Identify the preparation type.
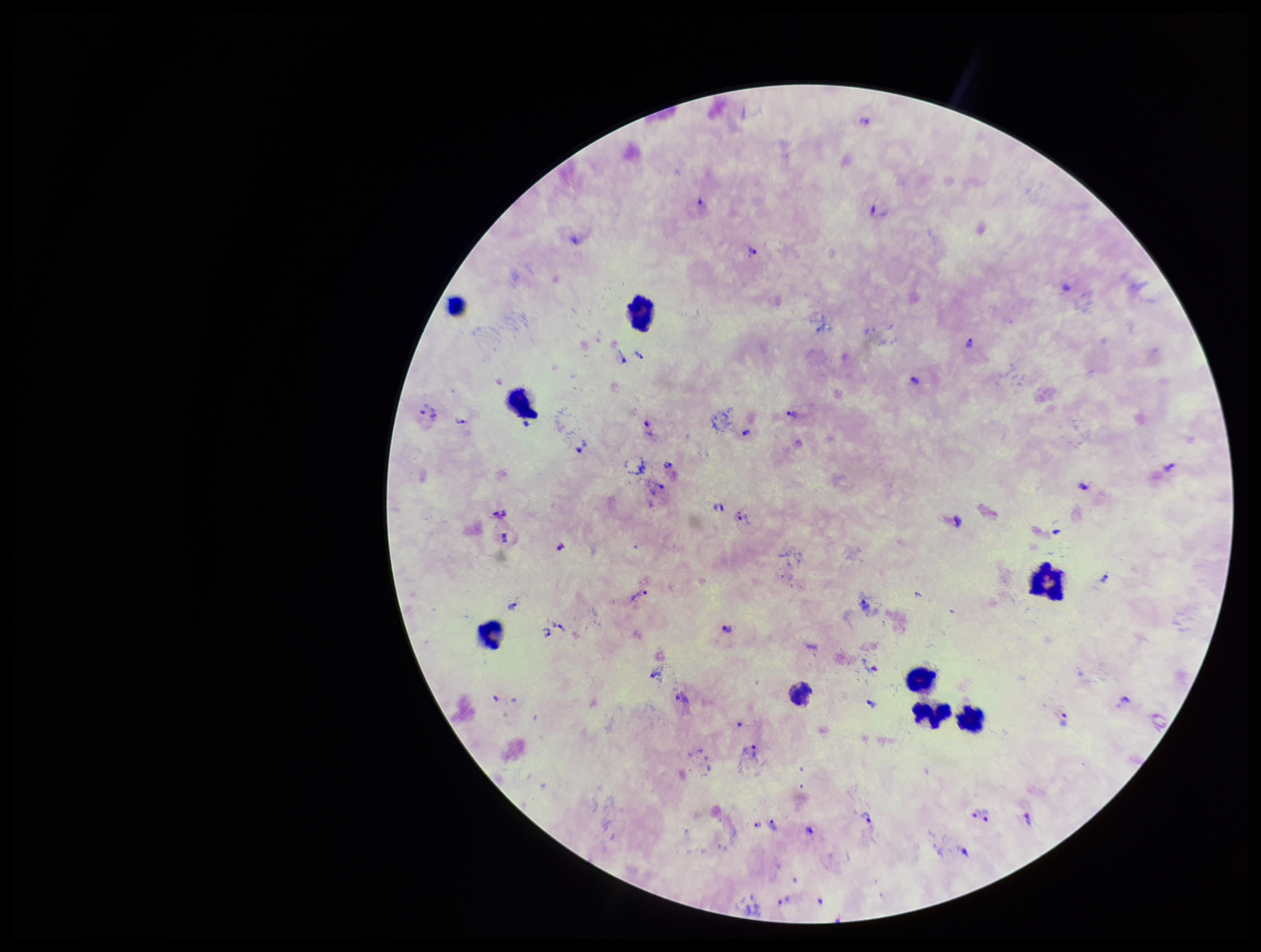
A thick smear.

Smartphone photograph taken through the eyepiece of a microscope. Plasmodium parasites: seen. Image is 1261×952 pixels. Parasite count: 41. Stained with Giemsa. Species reported for this patient: Plasmodium vivax. Leukocyte count: 9. Patient malaria status: positive. Single field of view.